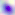
Summary:
  - Magnification: 400x
  - Identification: Toxoplasma gondii
  - Modality: photomicrograph